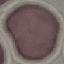
Summary:
  - Result: no malaria parasites seen
  - Capture: smartphone camera at the microscope eyepiece
  - Preparation: thin blood smear
  - Stain: Giemsa
  - Image type: automatically extracted cell patch, resized to 64 × 64 pixels